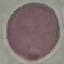

Result: negative for malaria parasites. Giemsa stain. Photographed with a smartphone camera at the microscope eyepiece. Thin blood film. Cell patch, automatically extracted from a larger field of view and resized to 64 × 64 pixels.